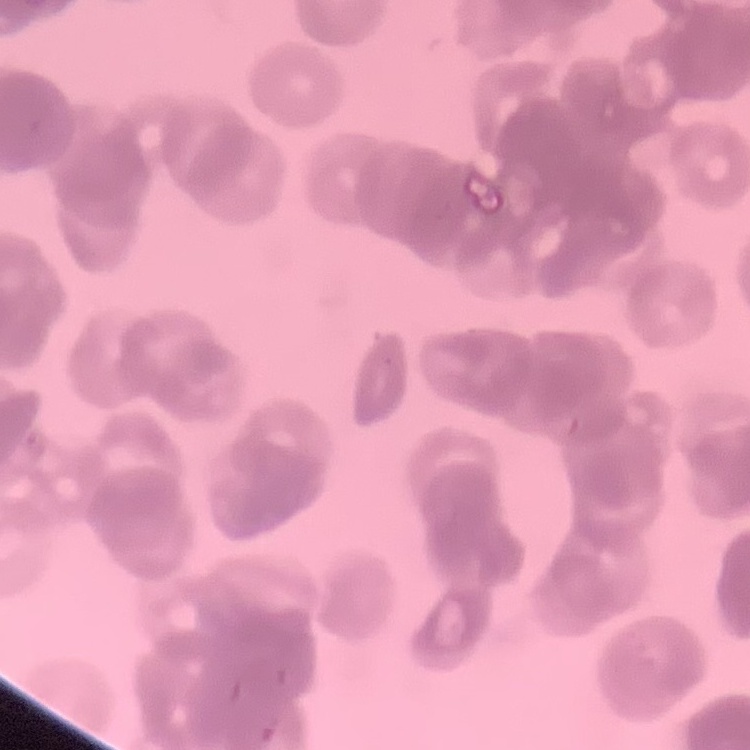
The erythrocytes show rouleaux formation. Thin blood film. One tile cut from a larger photomicrograph. Field's or Giemsa stain.